Describe the morphology of the red blood cells.
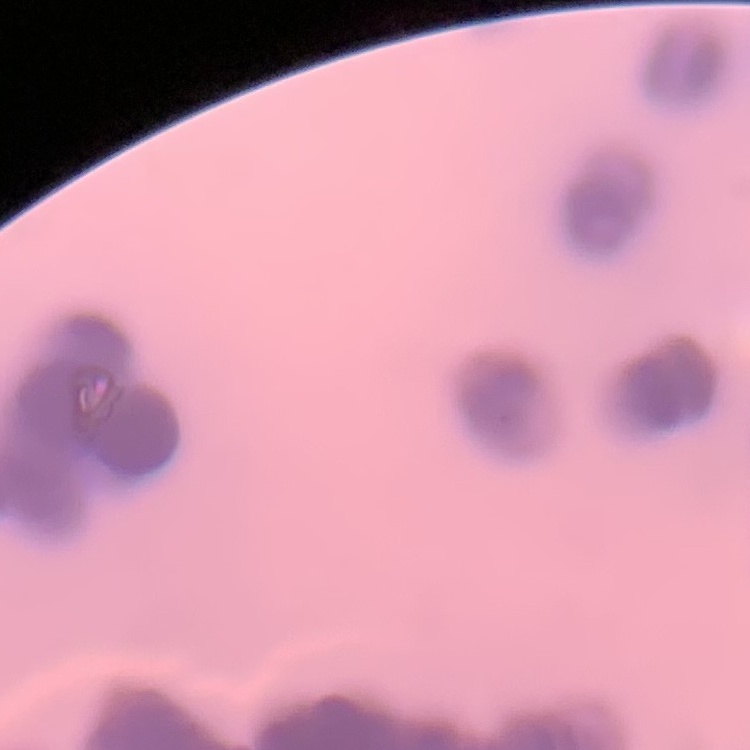
Rouleaux formation.

{
  "stain": "Field's or Giemsa",
  "preparation": "thin blood film",
  "image_type": "square crop of a larger photomicrograph"
}